Assess the morphology of the erythrocytes.
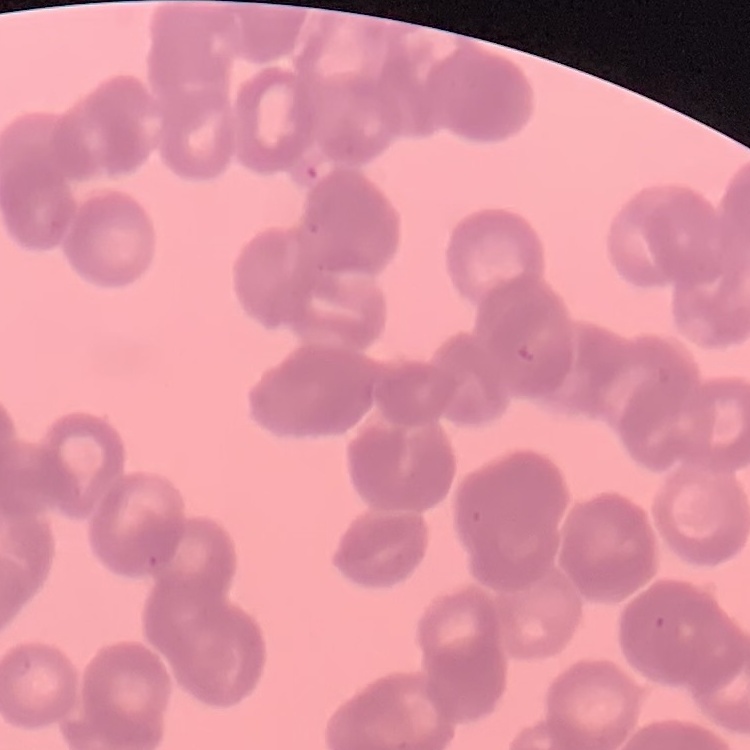

Rouleaux formation.

Summary:
  - Image type: square crop of a larger photomicrograph
  - Preparation: thin blood smear
  - Stain: Field's or Giemsa